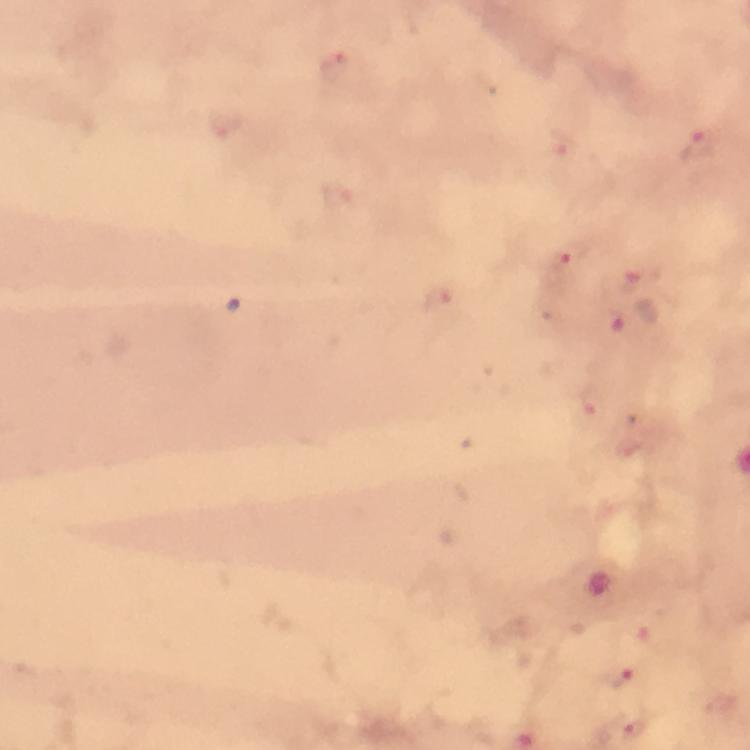
Approximate object centers, in pixels from the top-left corner.
Summary:
  - Plasmodium parasite locations: (x=339, y=67), (x=223, y=124), (x=564, y=142), (x=699, y=146), (x=341, y=201), (x=564, y=254), (x=633, y=283), (x=437, y=295), (x=593, y=404), (x=619, y=673), (x=630, y=720)
  - Magnification: 100x
  - Cropped from: one field of view
  - Stain: Giemsa
  - Capture: smartphone photograph through a microscope
  - Preparation: thick blood smear
  - Context: from a diagnostic examination for malaria
  - Image size: 750×750 pixels
  - Immersion oil: applied